State the preparation type.
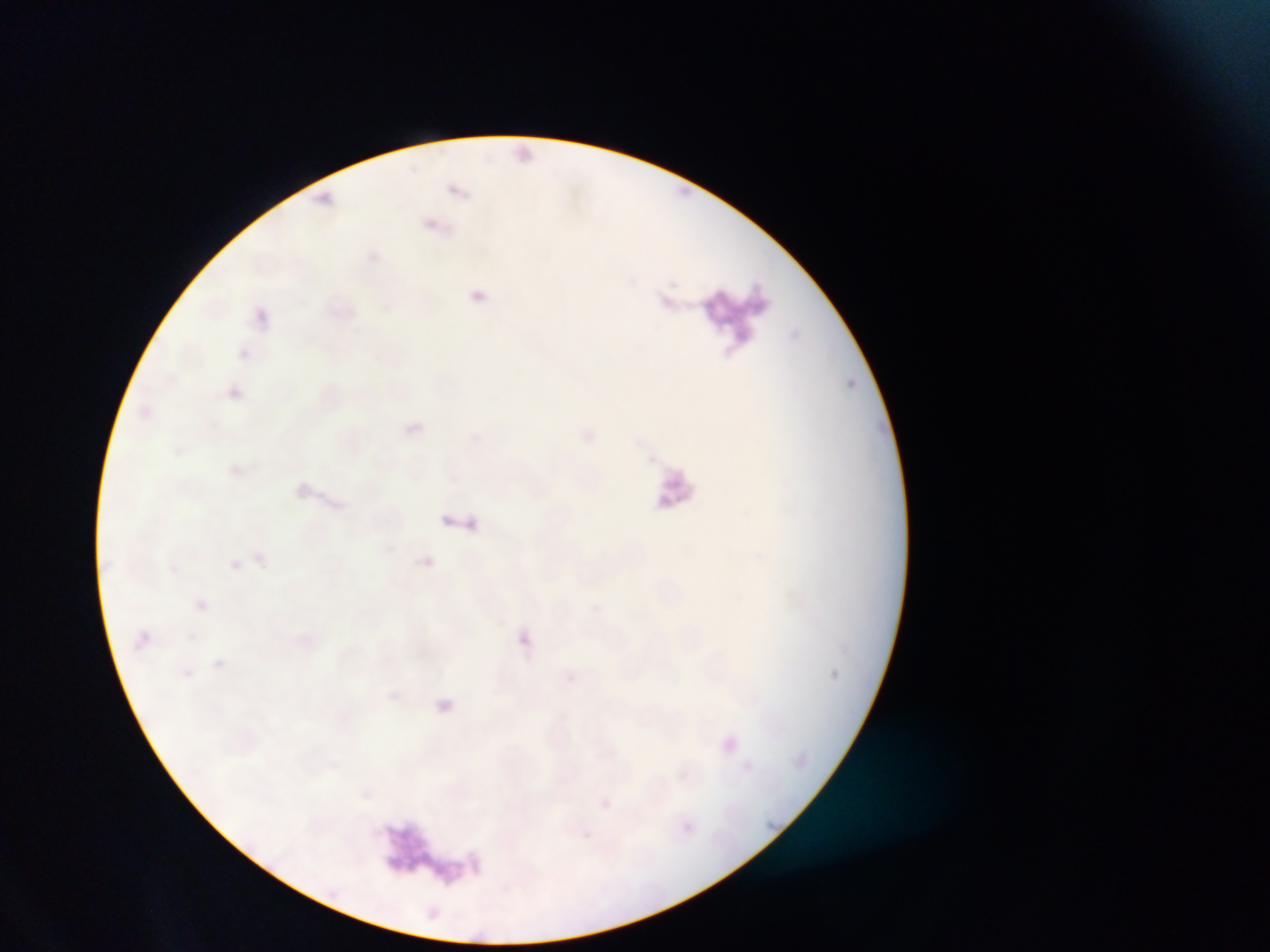
Thin blood film.

image size = 1270×952 pixels
capture = mobile-phone photograph through a microscope
field of view = single
artifact (stain precipitate or debris) locations = approximate bounding boxes as (left, top, right, bottom) in pixels: (690, 286, 792, 355), (647, 462, 716, 538), (384, 811, 461, 888)
Plasmodium parasite locations = approximate bounding boxes as (left, top, right, bottom) in pixels: (426, 220, 437, 231), (471, 290, 484, 301), (239, 348, 250, 359), (140, 406, 151, 419), (420, 554, 434, 568), (230, 558, 242, 570), (195, 599, 209, 611), (591, 602, 601, 611), (495, 618, 506, 628), (137, 631, 149, 644), (215, 659, 224, 668), (182, 668, 193, 678), (564, 671, 575, 680), (389, 691, 399, 701), (436, 699, 452, 712), (362, 789, 372, 799), (601, 799, 612, 808), (685, 824, 693, 832)
country = Ghana